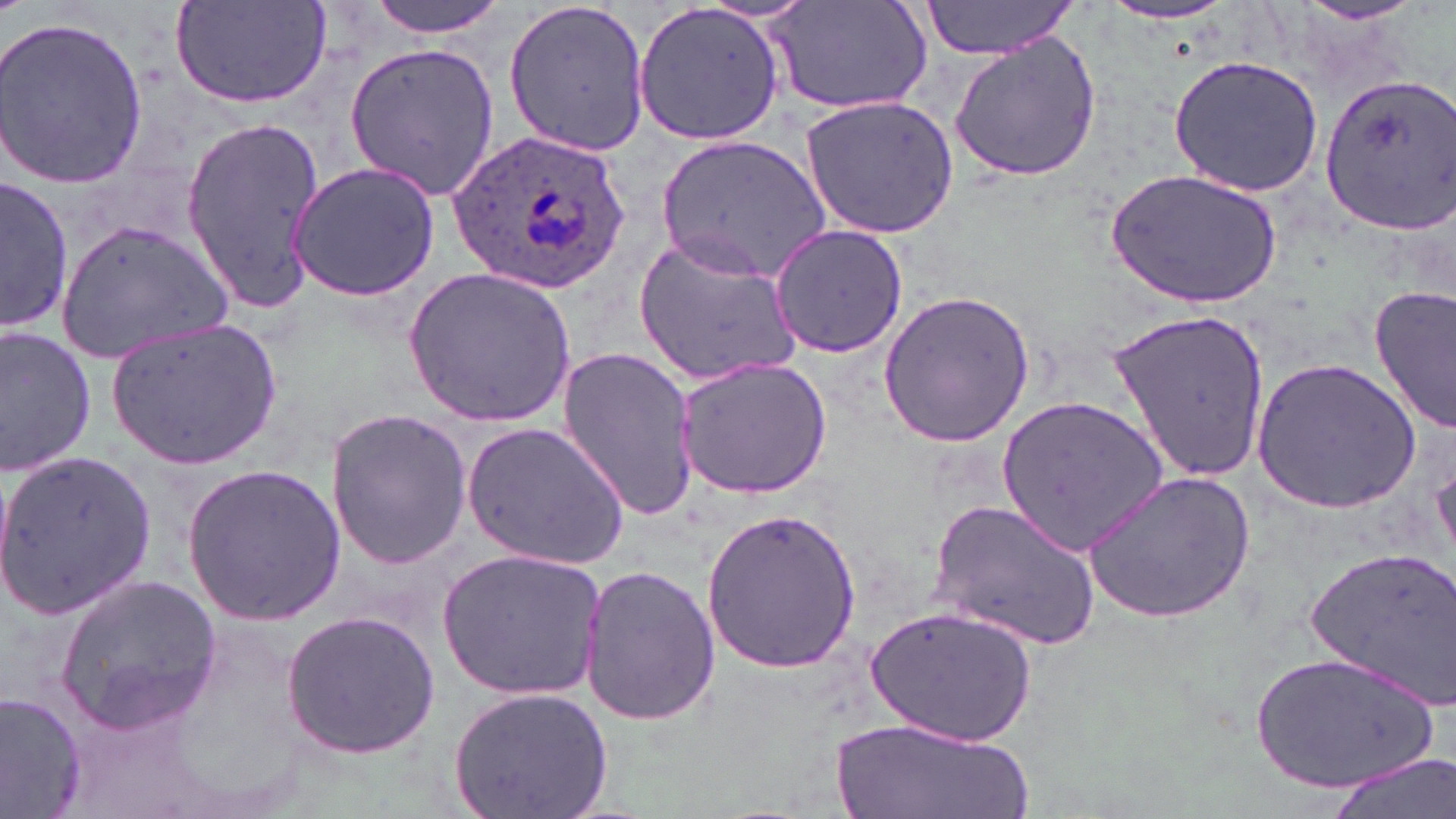
Summary:
  - Coordinate format: approximate bounding boxes as [x1, y1, x2, y2] in pixels
  - Uninfected red blood cell locations: [359, 0, 513, 36], [501, 0, 652, 156], [173, 1, 334, 112], [919, 1, 1084, 58], [767, 2, 934, 116], [1096, 2, 1247, 28], [633, 3, 784, 146], [1286, 3, 1434, 30], [0, 14, 151, 189], [947, 33, 1103, 183], [342, 41, 500, 198], [1168, 55, 1324, 195], [1315, 71, 1456, 233], [802, 95, 959, 237], [180, 118, 325, 315], [657, 135, 832, 279], [284, 161, 442, 303], [1108, 168, 1280, 309], [1, 176, 74, 334], [62, 215, 233, 365], [768, 224, 909, 360], [631, 229, 804, 388], [404, 265, 575, 427], [1370, 286, 1455, 433], [878, 288, 1035, 447], [1107, 308, 1272, 486], [102, 315, 287, 471], [0, 325, 98, 479], [553, 346, 701, 521], [674, 357, 831, 500], [1252, 358, 1422, 512], [996, 394, 1172, 556], [326, 406, 473, 572], [462, 420, 628, 568], [1, 449, 155, 621], [180, 463, 347, 630], [1084, 466, 1258, 624], [931, 497, 1101, 652], [699, 507, 860, 675], [1305, 544, 1455, 701], [437, 549, 607, 700], [577, 562, 722, 728], [54, 574, 222, 734], [870, 602, 1043, 752], [280, 608, 443, 761], [1247, 650, 1441, 795], [446, 684, 613, 819], [0, 687, 87, 819], [831, 718, 1034, 819], [1325, 753, 1455, 819]
  - Plasmodium ovale-infected red blood cell locations: [445, 128, 633, 297]
  - Slide-level diagnosis: Plasmodium ovale
  - Field of view: one of a larger specimen
  - Magnification: 1000x
  - Image size: 1456×819 pixels
  - Preparation: thin blood smear
  - Modality: optical microscopy
  - Stain: May-Grünwald-Giemsa